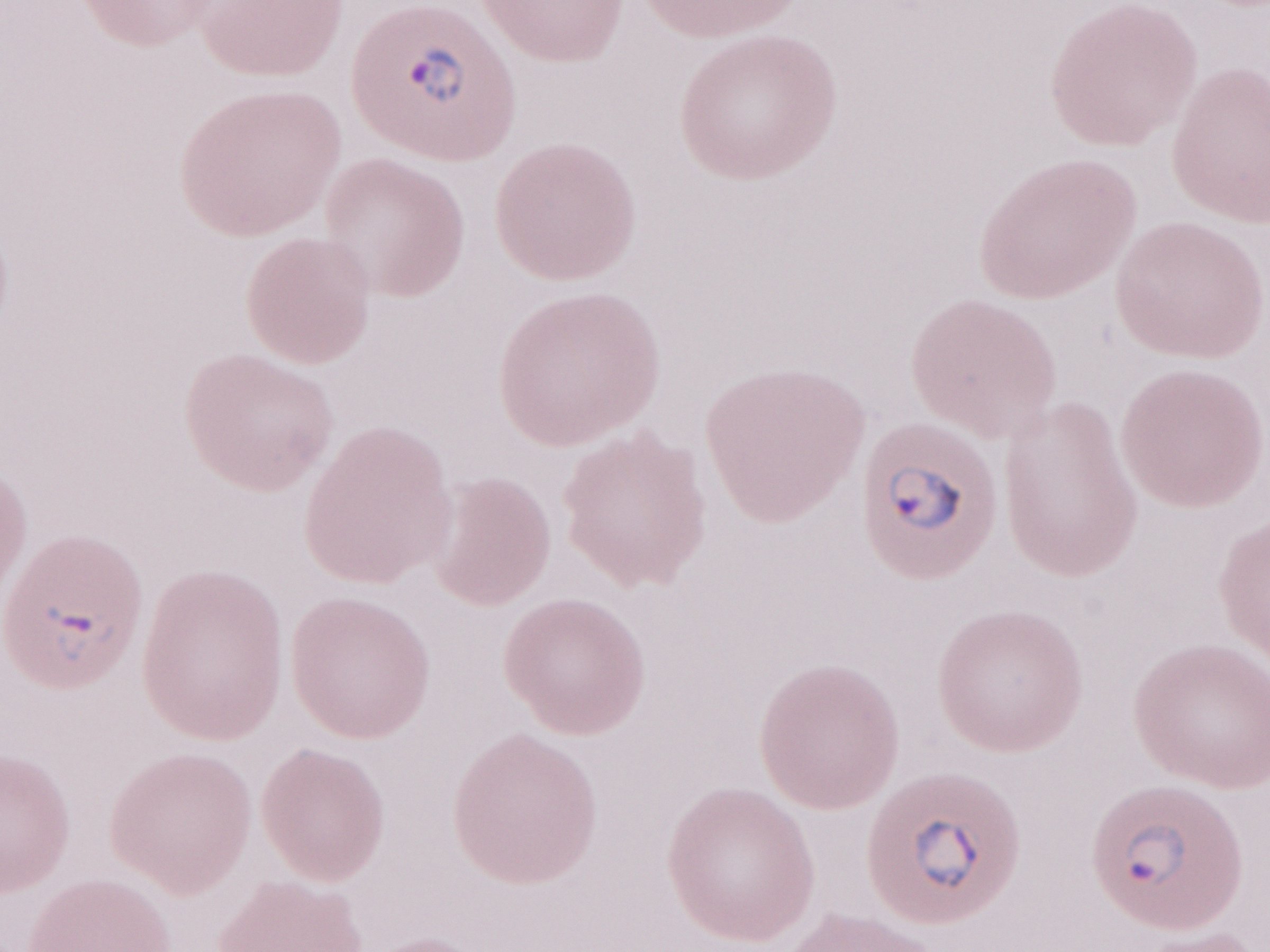 Image is 1270×952 pixels. Thin blood film. Olympus BX43 microscope and DP73 digital camera. One field of this slide. 1,000x magnification. Malaria diagnosis (patient-level): positive. May-Grünwald-Giemsa (MGG) stain.